Locate every leukocyte (white blood cell).
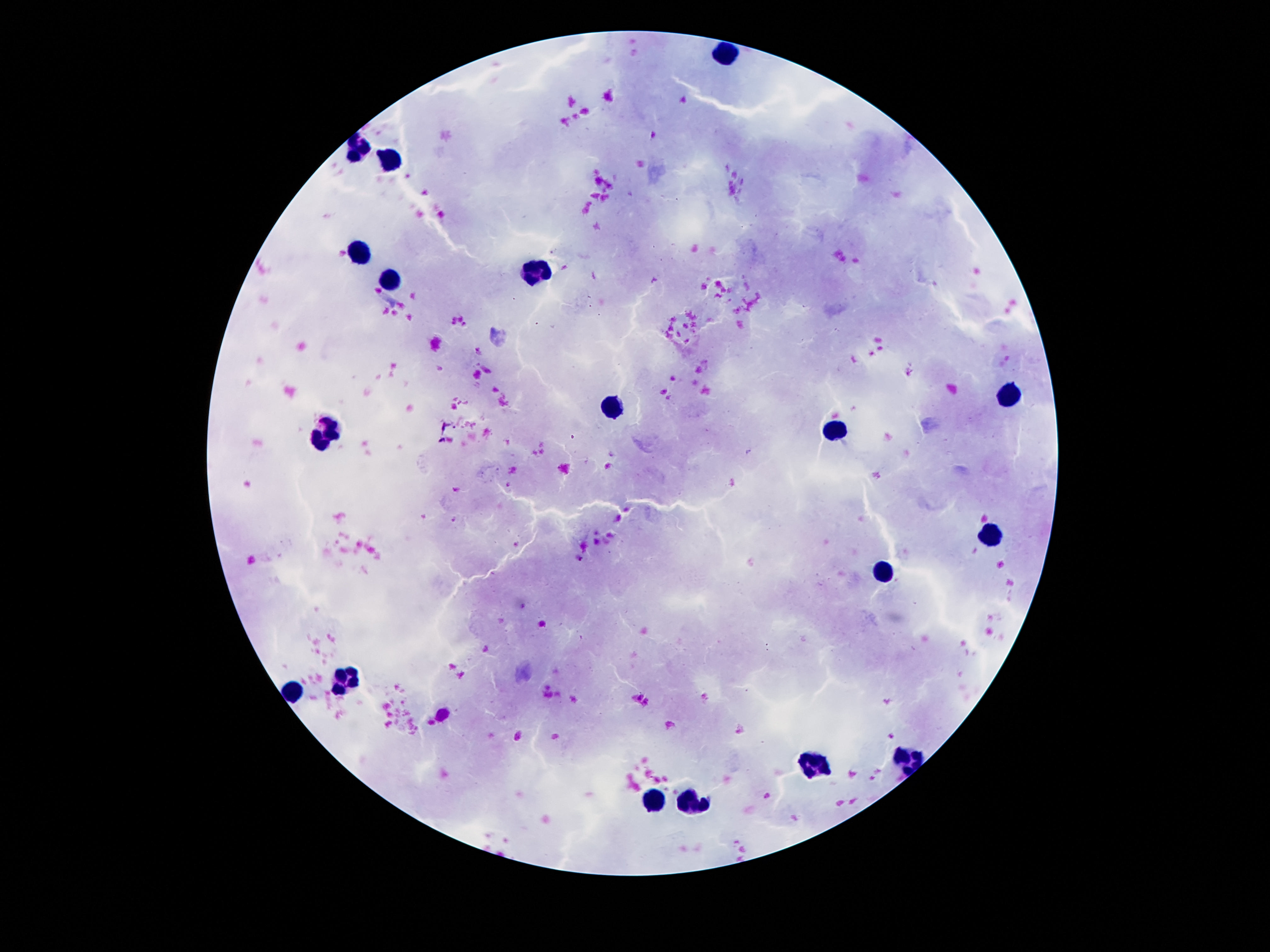

Approximate centers as (x, y) in pixels.
Leukocytes: (725, 55), (363, 148), (389, 164), (359, 251), (540, 273), (391, 283), (1007, 399), (611, 407), (326, 432), (835, 432), (993, 536), (883, 567), (349, 679), (294, 691), (905, 765), (812, 769), (653, 800), (690, 804).

Summary:
  - Stain: Giemsa
  - Preparation: thick blood smear
  - Magnification: 100x
  - Capture: smartphone camera through the microscope eyepiece
  - Patient malaria status: negative
  - Image size: 1270×952 pixels
  - Field of view: single